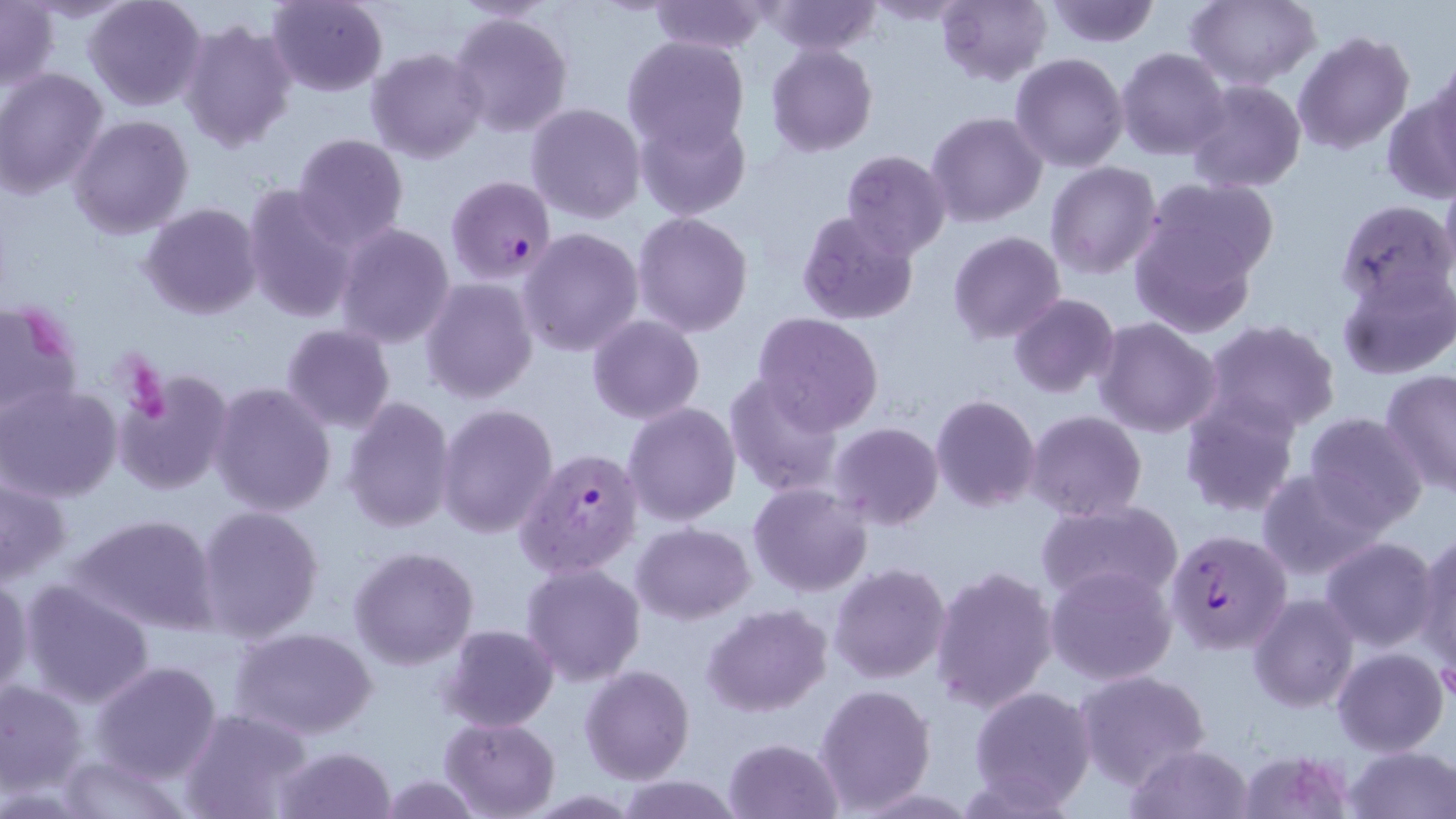
Summary:
  - Coordinate format: approximate bounding boxes as (x1,y1)-(x2,y2) corner pairs in pixels
  - Platelet locations: (130,360)-(173,425)
  - Uninfected red blood cell locations: (83,0)-(207,112), (266,0)-(387,96), (648,0)-(768,55), (936,0)-(1051,88), (1045,0)-(1161,48), (1183,0)-(1320,89), (759,1)-(884,56), (865,1)-(976,26), (1,2)-(58,89), (448,10)-(574,139), (179,16)-(297,152), (1293,30)-(1415,155), (620,35)-(750,155), (766,43)-(878,156), (367,47)-(488,164), (1117,48)-(1231,161), (1010,53)-(1129,173), (1424,57)-(1456,167), (0,68)-(108,200), (1186,80)-(1306,192), (1384,85)-(1456,200), (526,102)-(647,224), (634,109)-(751,222), (927,111)-(1047,228), (69,114)-(194,240), (291,133)-(409,249), (842,150)-(951,259), (1045,162)-(1162,278), (1137,175)-(1281,293), (241,183)-(360,323), (1334,199)-(1454,309), (139,204)-(262,320), (631,209)-(754,337), (795,209)-(919,325), (1128,210)-(1264,340), (334,223)-(455,348), (517,227)-(644,357), (949,231)-(1066,344), (1336,263)-(1454,381), (421,278)-(538,404), (1008,293)-(1119,398), (0,297)-(85,420), (753,312)-(884,432), (588,314)-(704,424), (1095,318)-(1222,439), (1201,319)-(1342,440), (281,323)-(395,434), (115,368)-(235,499), (1379,368)-(1455,497), (723,372)-(847,496), (1,381)-(122,503), (210,381)-(337,517), (931,393)-(1041,512), (340,395)-(457,534), (1178,396)-(1301,518), (624,402)-(741,527), (435,403)-(558,538), (1026,410)-(1148,524), (1303,413)-(1429,533), (830,423)-(944,529), (1256,467)-(1389,581), (0,472)-(73,586), (747,482)-(873,599), (1036,499)-(1183,606), (195,505)-(324,643), (69,512)-(222,635), (632,522)-(755,624), (1413,530)-(1456,675), (1319,536)-(1442,652), (348,545)-(479,670), (520,561)-(646,684), (829,562)-(952,685), (1045,564)-(1178,686), (930,565)-(1058,713), (0,574)-(32,700), (17,580)-(157,710), (1247,593)-(1360,712), (703,604)-(831,717), (440,625)-(560,731), (231,626)-(377,741), (1331,647)-(1450,757), (90,661)-(222,785), (580,665)-(695,784), (1074,669)-(1211,789), (1,679)-(88,795), (815,682)-(936,813), (968,684)-(1097,811), (179,709)-(315,819), (441,717)-(560,817), (725,738)-(843,819), (275,744)-(397,819), (1124,744)-(1250,818), (1342,744)-(1455,819), (57,749)-(189,819), (379,774)-(482,818), (614,775)-(744,818)
  - Plasmodium falciparum-infected red blood cell locations: (445,175)-(557,285), (515,446)-(645,579), (1164,529)-(1292,654)
  - Slide-level diagnosis: Plasmodium falciparum
  - Modality: optical microscopy
  - Preparation: thin blood smear
  - Image size: 1456×819 pixels
  - Stain: May-Grünwald-Giemsa
  - Magnification: 1000x
  - Field of view: one of a larger specimen